Assess this cell for malaria.
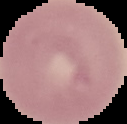

It is uninfected.

Summary:
  - Preparation: thin blood film
  - Image size: 127×124 pixels
  - Image type: cell region segmented out of the field of view; surrounding area masked to black